State which parasite is depicted.
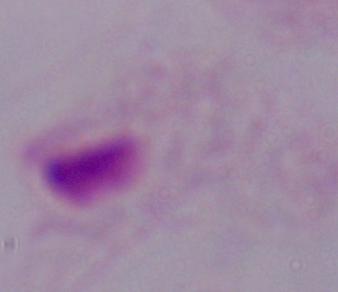

This is a trichomonad.

Micrograph. 1000x magnification.